Locate every Plasmodium parasite and every leukocyte.
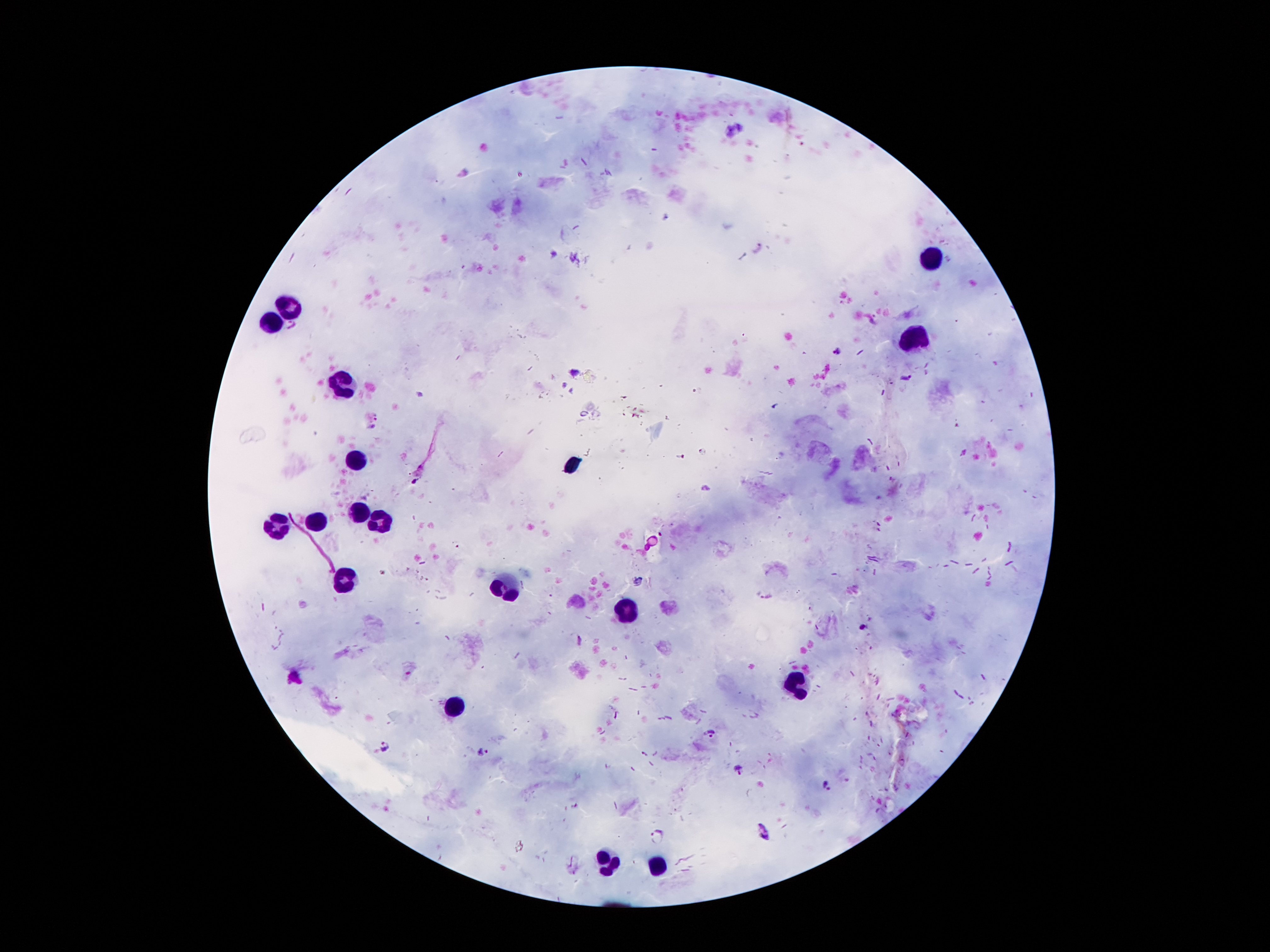
Approximate centers as [x, y] in pixels.
Plasmodium parasites: [836, 351], [906, 376], [764, 595], [709, 733], [386, 746], [484, 752], [738, 770], [829, 786], [764, 832], [658, 838].
Leukocytes: [935, 257], [290, 306], [268, 324], [920, 338], [339, 388], [357, 462], [359, 509], [377, 519], [317, 521], [275, 524], [344, 578], [505, 583], [626, 610], [799, 687], [453, 707], [609, 860], [661, 862].

Giemsa-stained preparation. 100x magnification. Photographed through the microscope eyepiece with a smartphone camera. Thick blood smear. Image is 1270×952 pixels. Patient malaria status: infected with Plasmodium falciparum. One field from this slide.